State the blood parasite species.
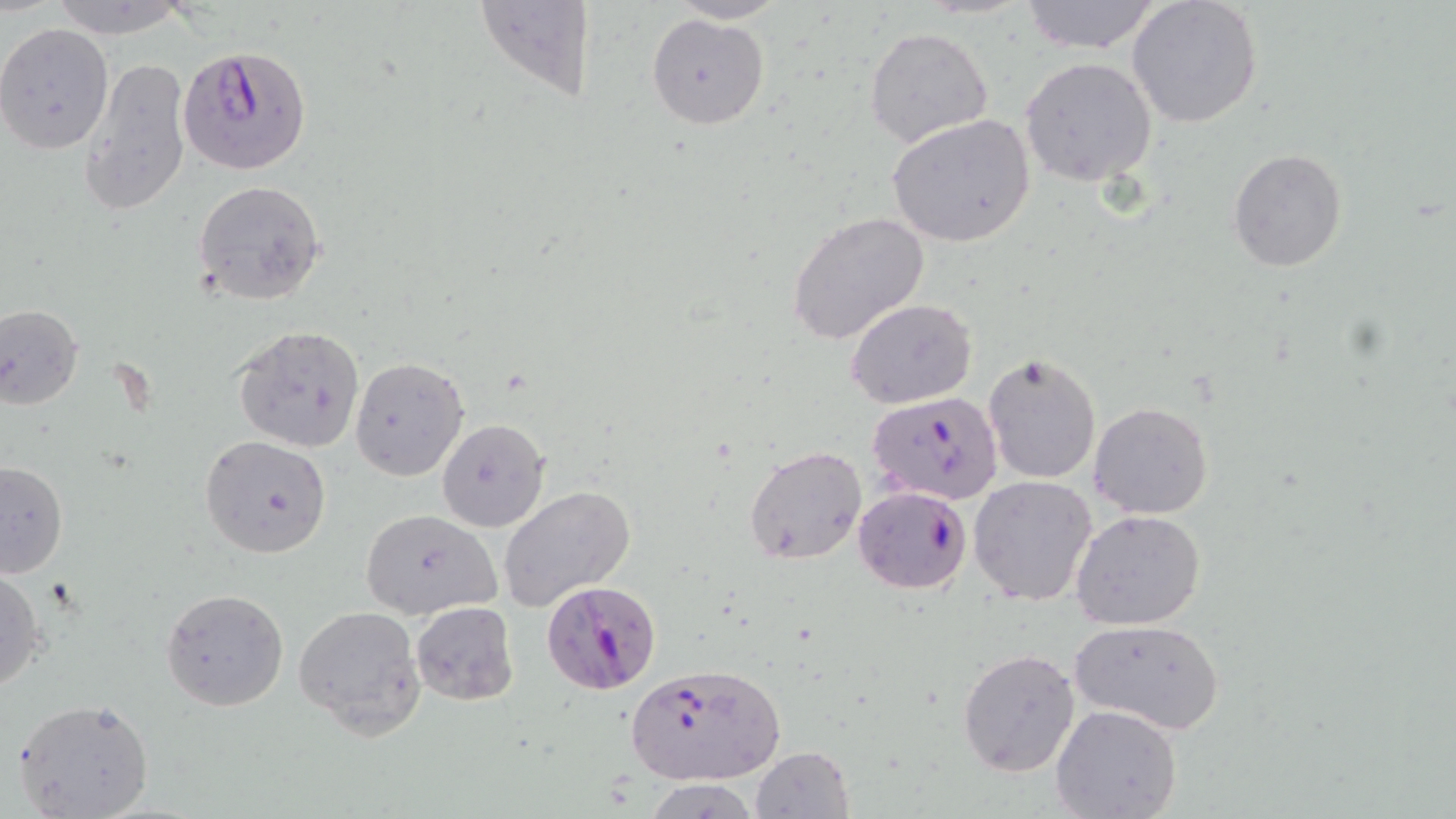

Plasmodium falciparum.

{
  "magnification": "1000x",
  "field_of_view": "single",
  "stain": "May-Grünwald-Giemsa",
  "plasmodium_falciparum_infected_red_blood_cell_locations": "approximate bounding boxes as named x1/y1/x2/y2 corners in pixels: (x1=178, y1=47, x2=312, y2=173), (x1=866, y1=392, x2=1003, y2=504), (x1=852, y1=485, x2=972, y2=595), (x1=542, y1=579, x2=663, y2=696), (x1=623, y1=663, x2=786, y2=785)",
  "modality": "optical microscopy",
  "preparation": "thin blood film",
  "uninfected_red_blood_cell_locations": "approximate bounding boxes as named x1/y1/x2/y2 corners in pixels: (x1=44, y1=0, x2=196, y2=39), (x1=472, y1=0, x2=595, y2=100), (x1=1018, y1=0, x2=1162, y2=53), (x1=667, y1=1, x2=789, y2=23), (x1=1126, y1=1, x2=1264, y2=130), (x1=646, y1=14, x2=768, y2=130), (x1=0, y1=23, x2=116, y2=156), (x1=865, y1=25, x2=995, y2=150), (x1=79, y1=55, x2=192, y2=221), (x1=1020, y1=57, x2=1159, y2=189), (x1=889, y1=113, x2=1034, y2=248), (x1=1226, y1=148, x2=1348, y2=272), (x1=191, y1=179, x2=328, y2=305), (x1=787, y1=211, x2=931, y2=345), (x1=845, y1=297, x2=977, y2=410), (x1=0, y1=303, x2=83, y2=409), (x1=234, y1=325, x2=366, y2=452), (x1=982, y1=351, x2=1103, y2=486), (x1=349, y1=356, x2=469, y2=481), (x1=1088, y1=401, x2=1214, y2=519), (x1=436, y1=417, x2=550, y2=532), (x1=198, y1=434, x2=331, y2=559), (x1=745, y1=446, x2=867, y2=565), (x1=0, y1=460, x2=70, y2=577), (x1=969, y1=476, x2=1099, y2=606), (x1=500, y1=484, x2=636, y2=611), (x1=1070, y1=508, x2=1207, y2=629), (x1=360, y1=509, x2=498, y2=618), (x1=0, y1=565, x2=47, y2=694), (x1=161, y1=589, x2=289, y2=711), (x1=411, y1=600, x2=519, y2=706), (x1=294, y1=605, x2=423, y2=736), (x1=1072, y1=618, x2=1224, y2=736), (x1=956, y1=646, x2=1080, y2=778), (x1=12, y1=697, x2=155, y2=819), (x1=1050, y1=703, x2=1183, y2=819), (x1=751, y1=745, x2=855, y2=819), (x1=645, y1=779, x2=761, y2=816)",
  "image_size": "1456×819 pixels"
}